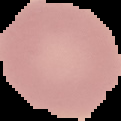
Image is 121×121 pixels. From a thin blood film. Malaria status: uninfected. Segmented cell region on a black background.